Locate Plasmodium parasites and leukocytes.
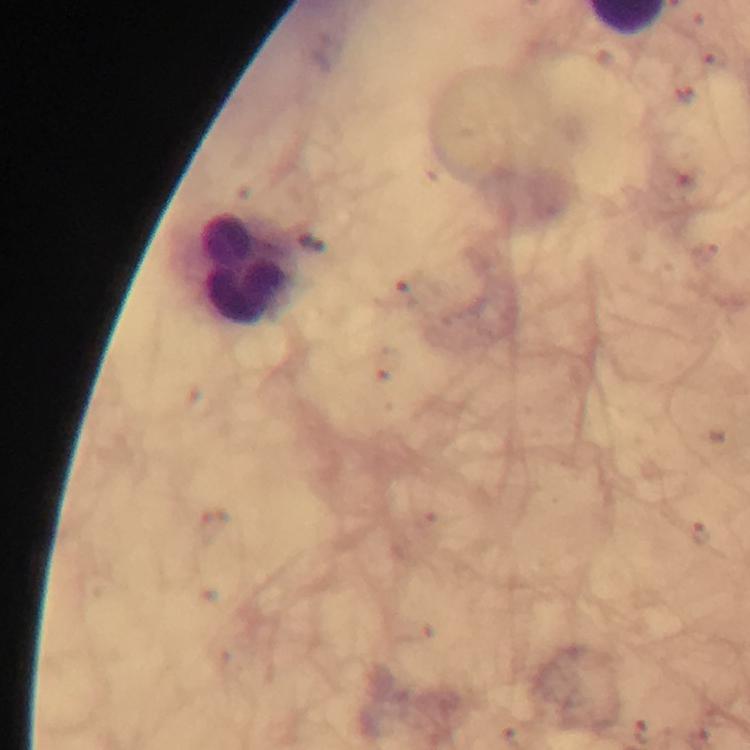
No Plasmodium parasites seen.
Approximate centers as (x, y) in pixels.
Leukocytes: (244, 268).

cropped from = a single field of view
capture = smartphone mounted on the microscope
preparation = thick blood smear
stain = Giemsa
context = from a diagnostic examination for malaria
magnification = 100x
immersion oil = applied
image size = 750×750 pixels